Describe the morphology of the red blood cells.
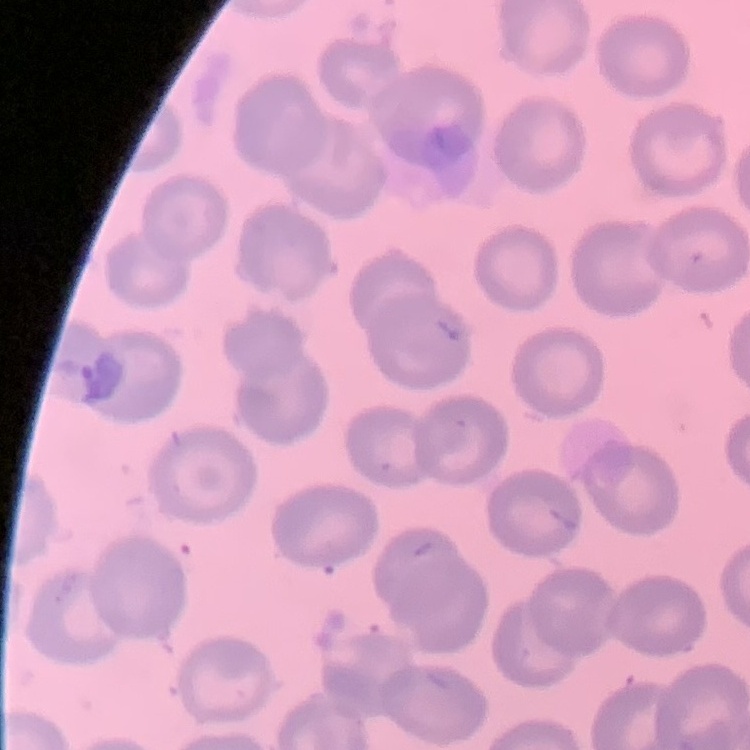

No rouleaux formation.

image_type: square crop of a larger photomicrograph
preparation: thin blood film
stain: Field's or Giemsa